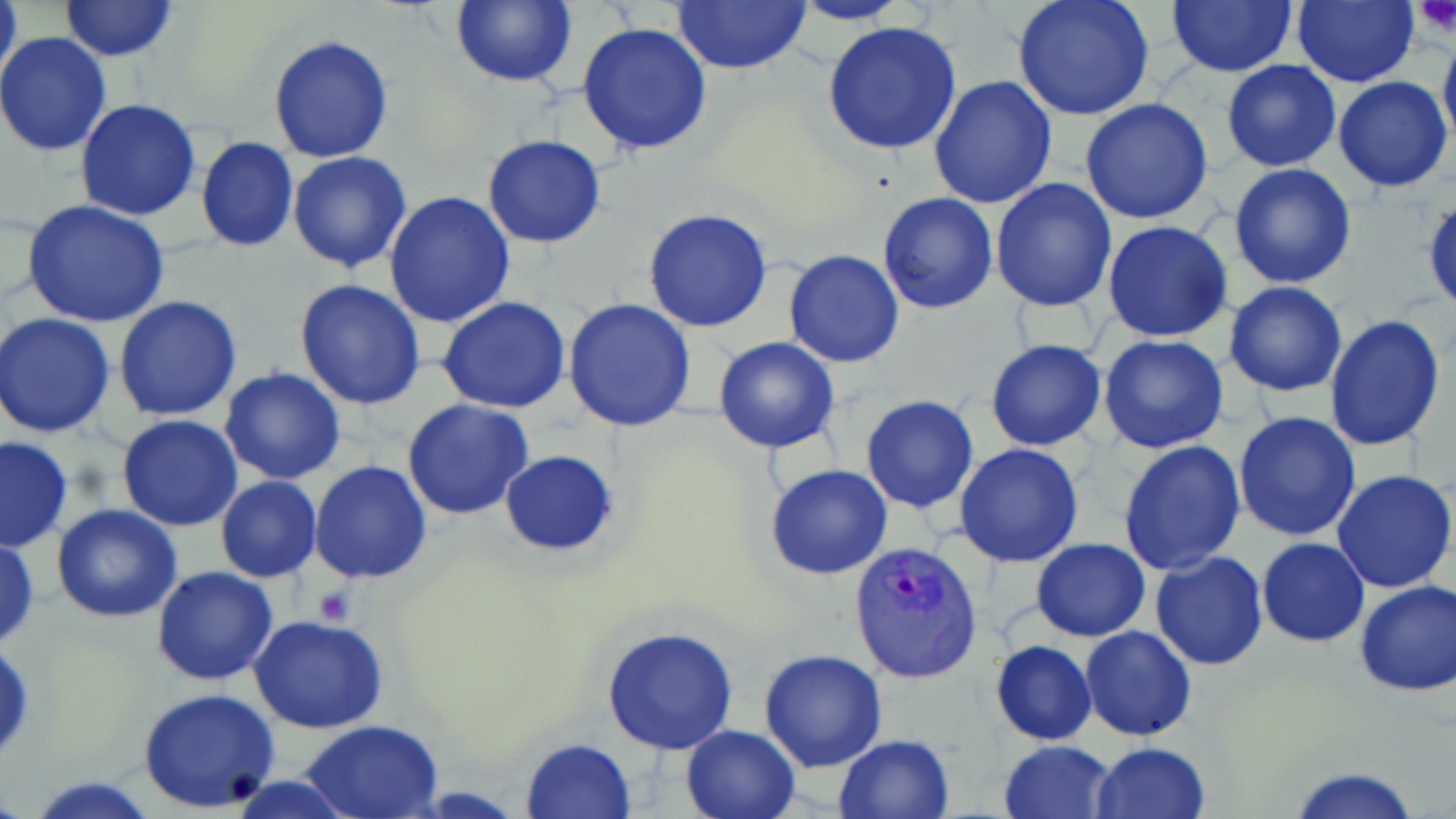
Approximate bounding boxes as named x1/y1/x2/y2 corners in pixels. Plasmodium vivax-infected red blood cell locations: (x1=849, y1=540, x2=983, y2=685). Uninfected red blood cell locations: (x1=1, y1=0, x2=20, y2=92), (x1=449, y1=0, x2=577, y2=87), (x1=671, y1=0, x2=812, y2=75), (x1=1011, y1=0, x2=1155, y2=122), (x1=1165, y1=0, x2=1297, y2=77), (x1=1293, y1=0, x2=1420, y2=87), (x1=57, y1=1, x2=179, y2=62), (x1=787, y1=1, x2=910, y2=25), (x1=822, y1=20, x2=962, y2=156), (x1=577, y1=22, x2=714, y2=156), (x1=0, y1=32, x2=114, y2=157), (x1=268, y1=34, x2=393, y2=163), (x1=1439, y1=35, x2=1456, y2=156), (x1=1222, y1=59, x2=1342, y2=172), (x1=928, y1=76, x2=1059, y2=210), (x1=1333, y1=76, x2=1453, y2=192), (x1=1081, y1=98, x2=1214, y2=224), (x1=76, y1=99, x2=201, y2=222), (x1=196, y1=137, x2=299, y2=254), (x1=482, y1=137, x2=606, y2=247), (x1=288, y1=152, x2=413, y2=275), (x1=1228, y1=163, x2=1357, y2=288), (x1=989, y1=178, x2=1118, y2=312), (x1=384, y1=191, x2=516, y2=327), (x1=877, y1=192, x2=998, y2=314), (x1=1423, y1=195, x2=1456, y2=317), (x1=22, y1=200, x2=170, y2=328), (x1=0, y1=204, x2=59, y2=309), (x1=643, y1=208, x2=773, y2=332), (x1=1102, y1=220, x2=1234, y2=342), (x1=784, y1=249, x2=906, y2=368), (x1=293, y1=279, x2=426, y2=410), (x1=1224, y1=282, x2=1347, y2=398), (x1=113, y1=297, x2=243, y2=421), (x1=437, y1=297, x2=571, y2=415), (x1=563, y1=299, x2=696, y2=432), (x1=0, y1=305, x2=231, y2=426), (x1=1, y1=312, x2=116, y2=437), (x1=1324, y1=312, x2=1447, y2=452), (x1=1098, y1=334, x2=1230, y2=455), (x1=713, y1=337, x2=839, y2=454), (x1=986, y1=339, x2=1108, y2=452), (x1=219, y1=367, x2=346, y2=484), (x1=860, y1=394, x2=979, y2=513), (x1=402, y1=399, x2=534, y2=520), (x1=1233, y1=410, x2=1363, y2=542), (x1=116, y1=415, x2=243, y2=532), (x1=0, y1=435, x2=73, y2=555), (x1=1118, y1=440, x2=1247, y2=577), (x1=954, y1=444, x2=1085, y2=567), (x1=499, y1=450, x2=619, y2=554), (x1=310, y1=461, x2=433, y2=585), (x1=765, y1=465, x2=893, y2=581), (x1=1331, y1=469, x2=1456, y2=593), (x1=216, y1=476, x2=321, y2=582), (x1=51, y1=504, x2=184, y2=622), (x1=0, y1=534, x2=40, y2=651), (x1=1258, y1=537, x2=1369, y2=646), (x1=1032, y1=538, x2=1151, y2=642), (x1=1150, y1=552, x2=1268, y2=671), (x1=150, y1=565, x2=278, y2=685), (x1=1354, y1=579, x2=1456, y2=695), (x1=248, y1=615, x2=389, y2=734), (x1=602, y1=626, x2=739, y2=756), (x1=1080, y1=626, x2=1197, y2=742), (x1=991, y1=640, x2=1097, y2=745), (x1=760, y1=648, x2=888, y2=772), (x1=136, y1=688, x2=282, y2=813), (x1=300, y1=719, x2=447, y2=817), (x1=680, y1=723, x2=802, y2=819), (x1=833, y1=734, x2=953, y2=818), (x1=519, y1=738, x2=637, y2=819), (x1=998, y1=740, x2=1120, y2=819), (x1=1090, y1=742, x2=1210, y2=819), (x1=1286, y1=763, x2=1425, y2=819), (x1=25, y1=775, x2=162, y2=817), (x1=222, y1=775, x2=362, y2=819). Platelet locations: (x1=1413, y1=0, x2=1455, y2=36), (x1=312, y1=585, x2=355, y2=625). Slide-level diagnosis: Plasmodium vivax. May-Grünwald-Giemsa-stained preparation. Thin blood smear. Image is 1456×819 pixels. Single field of view. Light microscopy. 1000x magnification.